Classify this cell by malaria status.
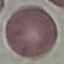

It is uninfected.

Automatically extracted cell patch, resized to 64 × 64 pixels. Giemsa stain. Acquired by smartphone through the microscope eyepiece. Thin blood smear.